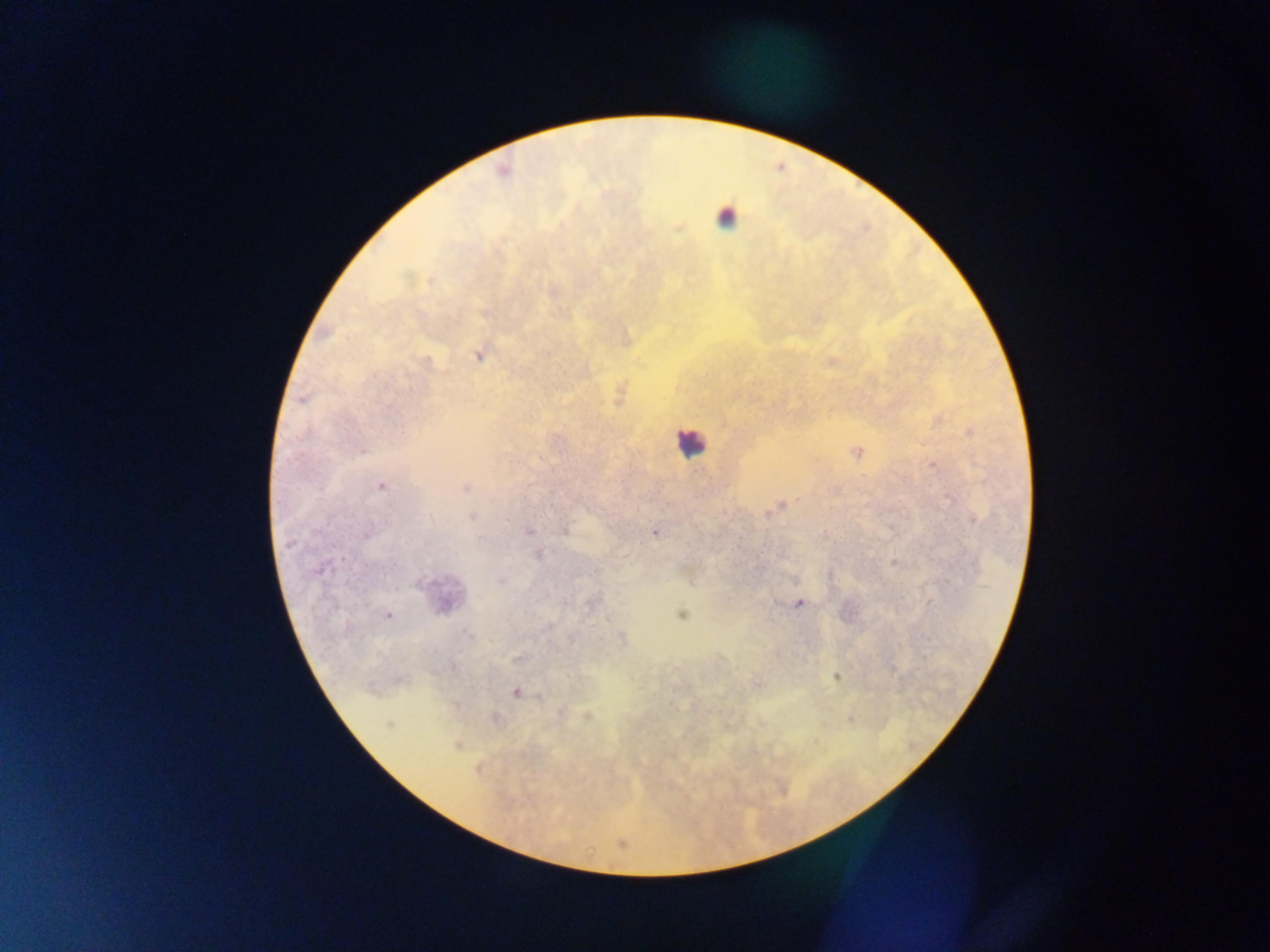 Approximate centers as x y in pixels. Leukocyte locations: 725 217; 689 442; 440 595. Plasmodium parasite locations: 503 170; 677 228; 485 312; 625 338; 480 354; 830 360; 619 393; 302 399; 937 418; 970 431; 855 452; 931 464; 381 485; 465 487; 778 506; 472 517; 973 519; 431 520; 528 531; 655 531; 366 534; 538 552; 895 562; 592 601; 798 602; 681 614; 387 615; 621 637; 519 658; 836 676; 756 685; 516 691; 539 696; 560 711; 586 716; 495 718; 850 718; 389 723; 456 744; 478 768; 620 843. Photographed through a microscope with a mobile-phone camera. Image is 1270×952 pixels. Single field of view. Thick blood film. Sample from Ghana.